Locate every Plasmodium falciparum parasite and give its life-cycle stage, and locate every leukocyte and any debris.
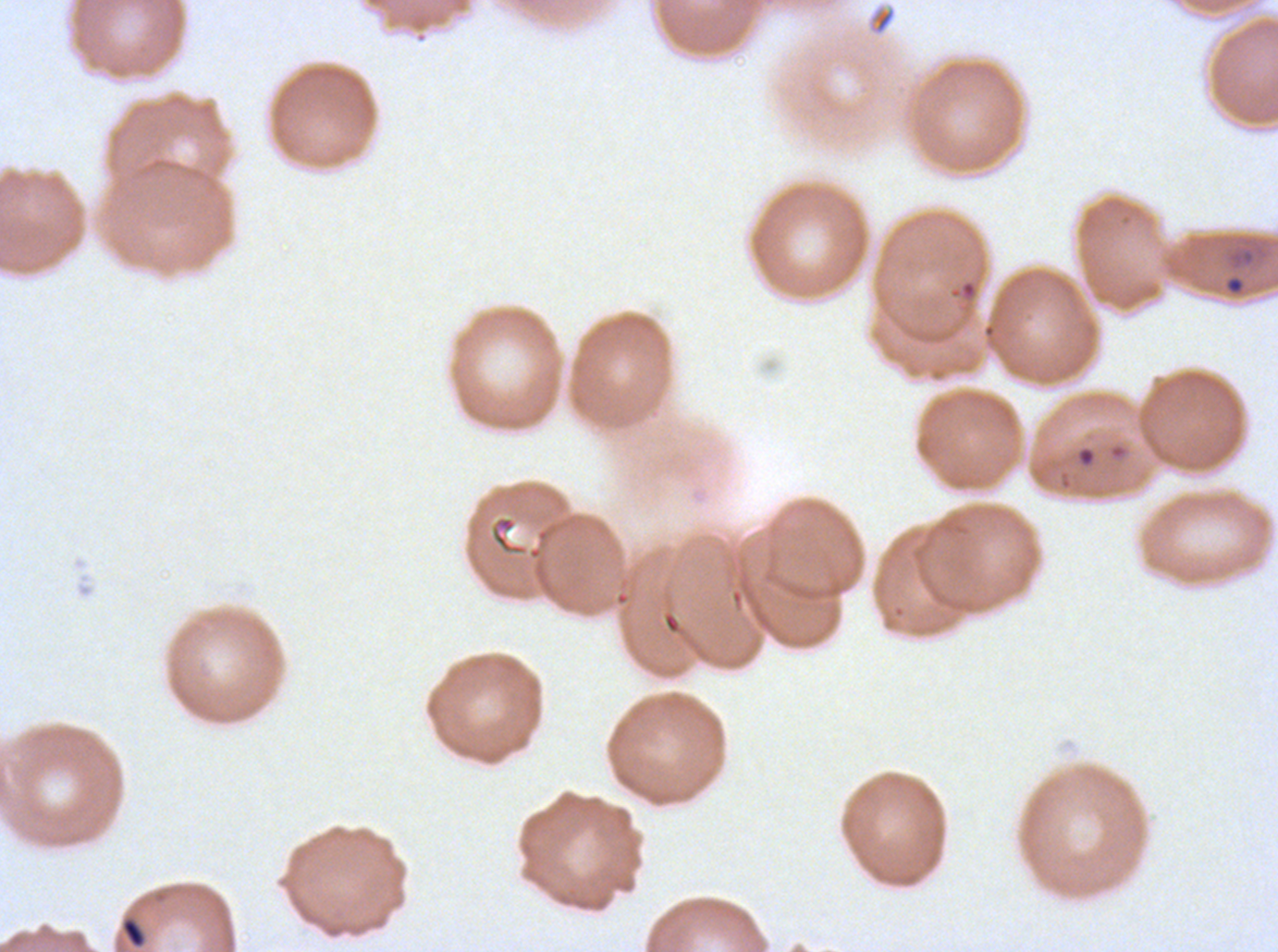
Approximate bounding boxes as {x1, y1, x2, y2} in pixels.
Rings: {1226, 276, 1244, 294}, {1076, 445, 1096, 468}.
Debris: {866, 6, 897, 36}, {120, 917, 147, 948}.
No late-ring/early-trophozoite forms, mid trophozoites, late trophozoites, early schizonts, late schizonts, segmenters, gametocytes, or leukocytes observed.

Summary:
  - Specimen: Plasmodium falciparum cultured ex vivo for 24 to 48 hours, from a patient in The Gambia
  - Stain: Giemsa
  - Image size: 1278×952 pixels
  - Preparation: thin blood film
  - Field of view: sub-image separated from a larger composite